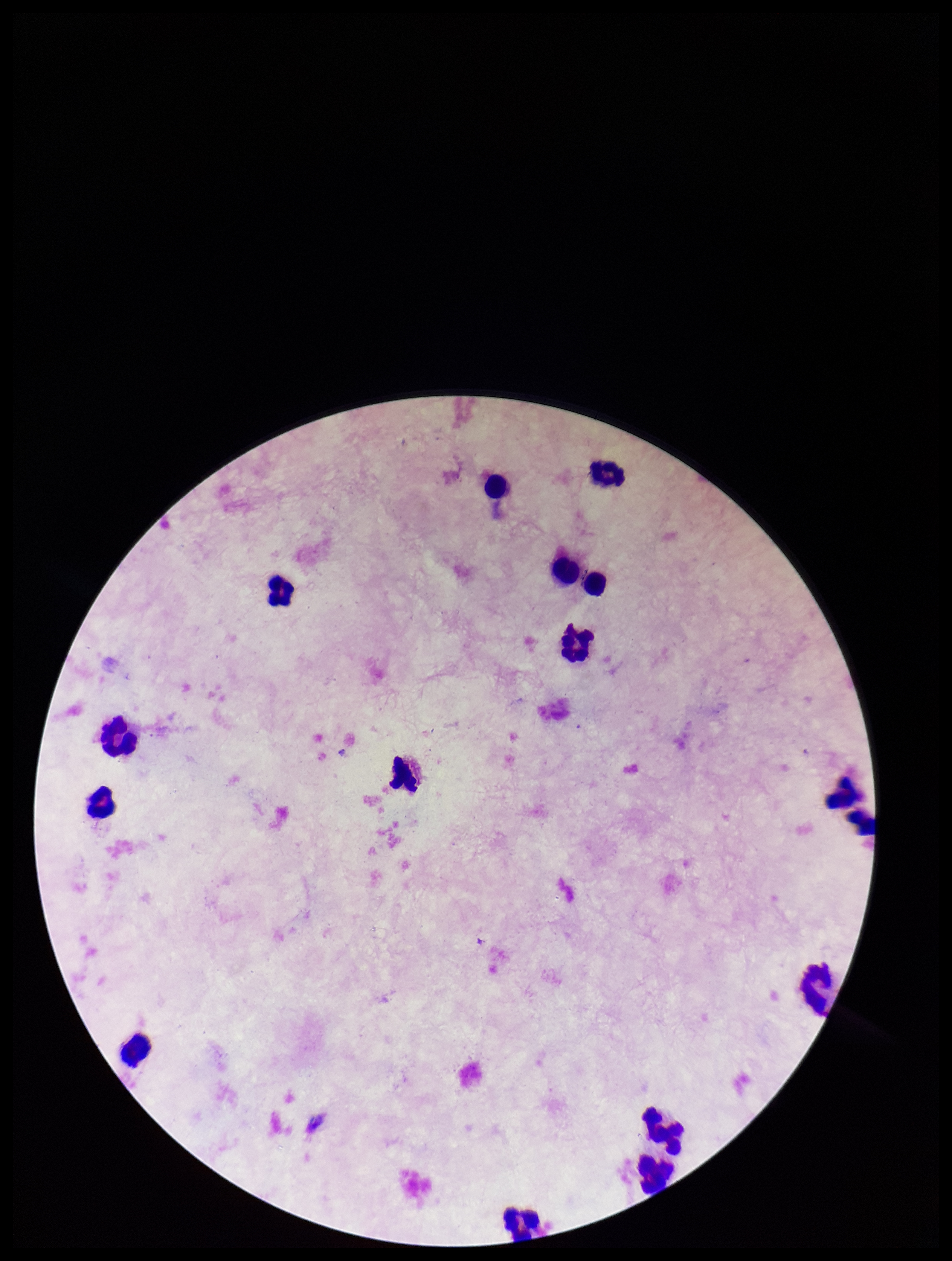
Stained with Giemsa. Smartphone photograph taken through the eyepiece of a microscope. Single field of view. Plasmodium parasites: none detected. Patient malaria status: negative. Preparation: thick smear. Leukocyte count: 16. Image is 952×1261 pixels. Parasite count: 0.